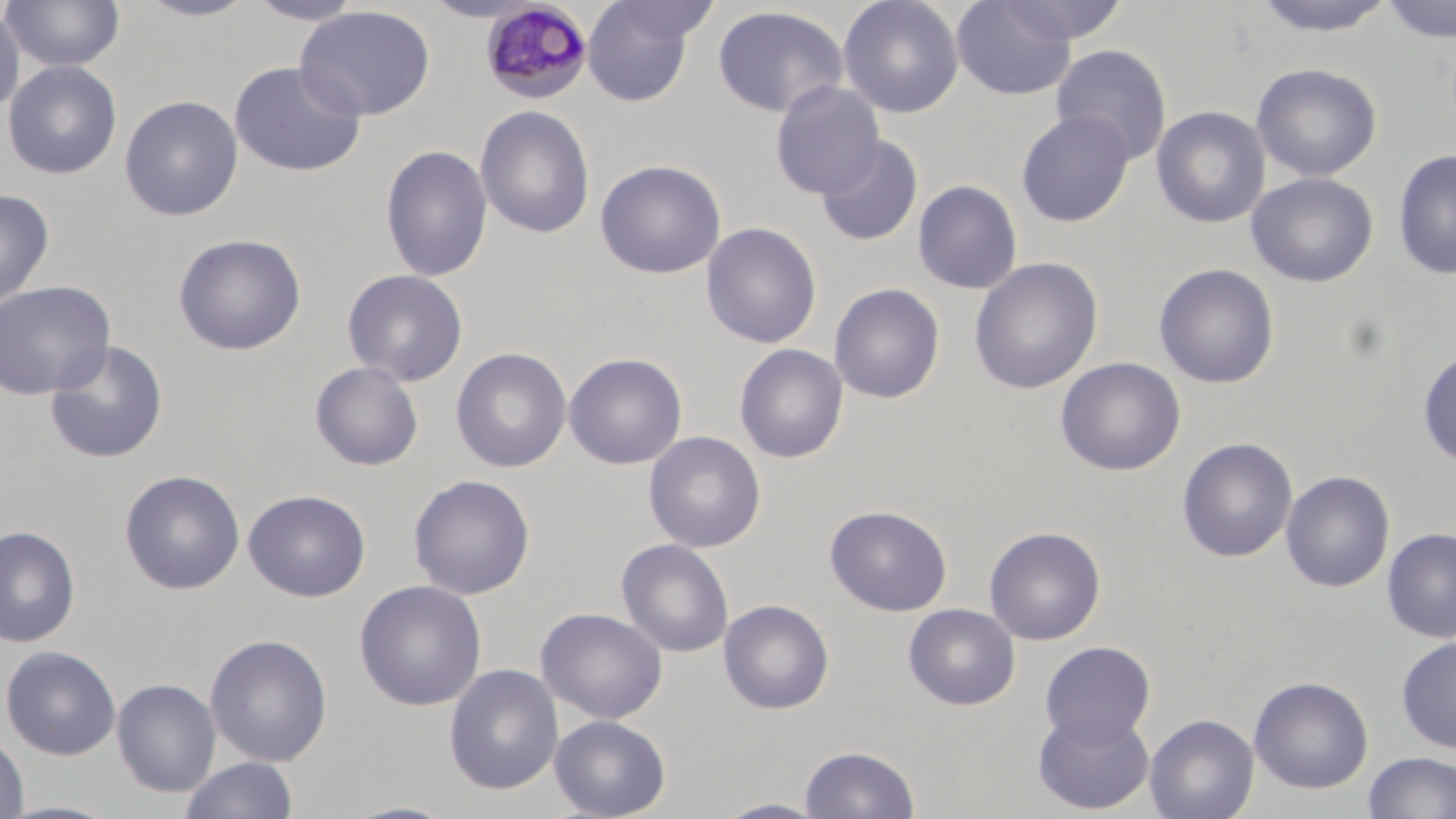
Summary:
  - Coordinate format: approximate bounding boxes as (x1, y1, x2, y2) in pixels
  - Uninfected red blood cell locations: (2, 0, 125, 74), (135, 0, 262, 22), (246, 0, 366, 25), (421, 0, 543, 22), (838, 0, 964, 118), (994, 0, 1129, 46), (1250, 0, 1398, 37), (1381, 0, 1456, 43), (582, 1, 701, 106), (952, 1, 1077, 99), (0, 4, 25, 119), (294, 5, 435, 122), (712, 5, 849, 118), (1050, 44, 1172, 165), (3, 60, 122, 180), (228, 60, 366, 177), (1251, 62, 1383, 182), (770, 80, 886, 199), (119, 95, 243, 221), (475, 104, 595, 239), (1151, 105, 1271, 229), (1016, 109, 1135, 227), (816, 136, 923, 247), (380, 144, 493, 282), (1393, 150, 1456, 280), (594, 159, 726, 279), (1246, 171, 1379, 288), (913, 179, 1023, 295), (0, 188, 54, 310), (701, 222, 822, 349), (173, 233, 307, 356), (968, 257, 1104, 395), (1154, 262, 1279, 389), (342, 269, 468, 385), (0, 280, 115, 400), (829, 283, 945, 403), (44, 339, 169, 464), (734, 343, 848, 463), (1417, 346, 1456, 468), (451, 347, 572, 473), (563, 352, 687, 470), (1056, 357, 1186, 476), (310, 361, 424, 471), (643, 431, 766, 553), (1177, 437, 1297, 562), (120, 469, 245, 595), (1281, 470, 1395, 593), (409, 474, 535, 599), (243, 489, 370, 602), (825, 505, 952, 616), (0, 525, 81, 648), (984, 525, 1106, 645), (1381, 527, 1456, 643), (616, 538, 734, 658), (354, 579, 487, 711), (718, 599, 834, 714), (903, 603, 1020, 710), (536, 607, 668, 724), (205, 633, 332, 766), (1395, 635, 1456, 753), (1040, 640, 1156, 747), (1, 645, 120, 759), (443, 664, 563, 795), (1249, 675, 1374, 794), (112, 678, 220, 797), (1033, 708, 1155, 815), (1145, 714, 1259, 819), (549, 715, 670, 818), (0, 732, 29, 819), (799, 745, 920, 818), (1361, 751, 1456, 819), (179, 756, 298, 819), (711, 798, 831, 818), (1, 800, 124, 819), (337, 800, 460, 819)
  - Plasmodium malariae-infected red blood cell locations: (480, 2, 593, 104)
  - Slide-level diagnosis: Plasmodium malariae
  - Field of view: single
  - Image size: 1456×819 pixels
  - Modality: light microscopy
  - Stain: May-Grünwald-Giemsa
  - Preparation: thin blood smear
  - Magnification: 1000x